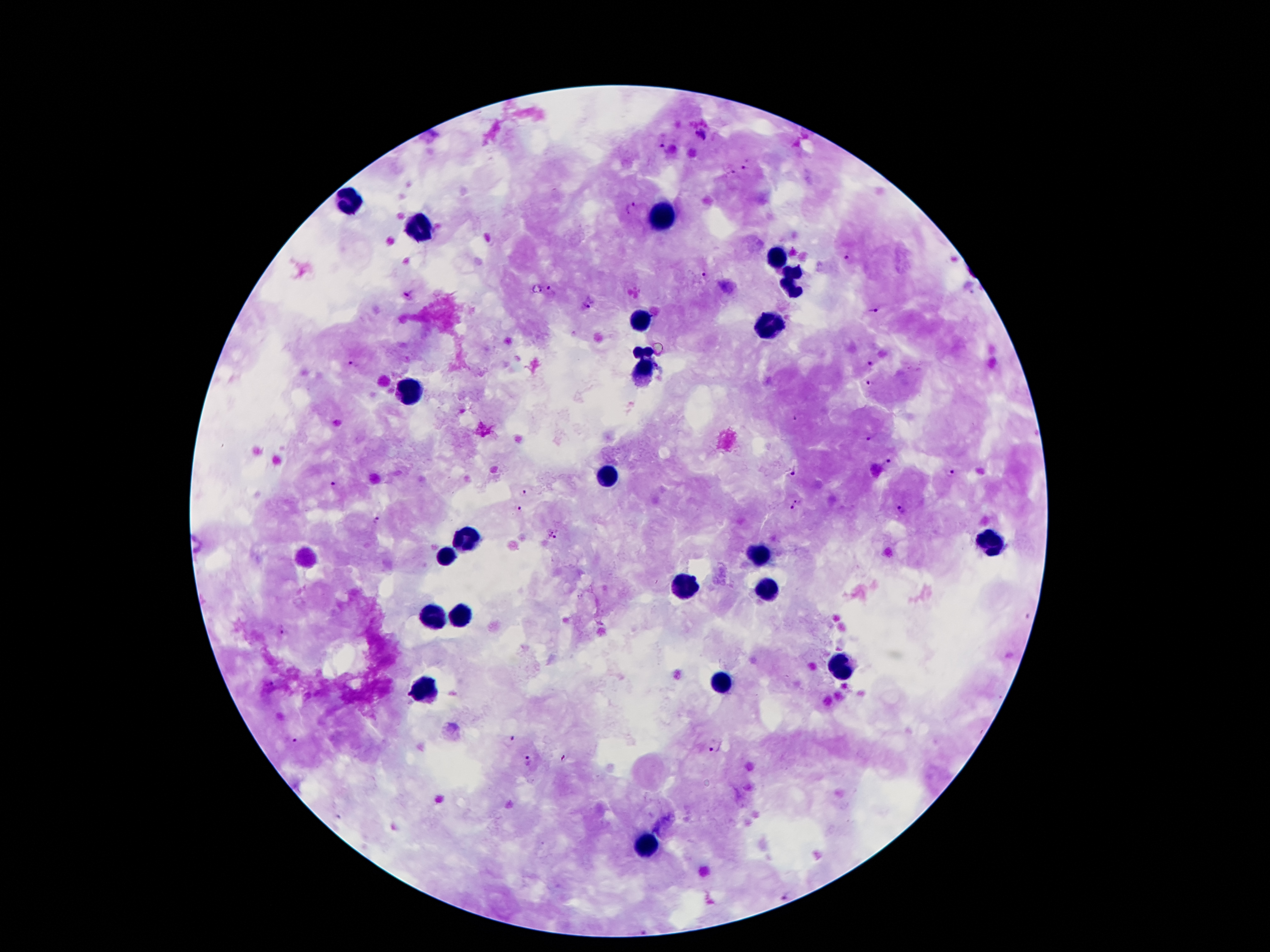
Approximate centers as {x, y} in pixels.
Summary:
  - Leukocyte locations: {349, 205}, {663, 218}, {417, 225}, {778, 257}, {797, 279}, {643, 320}, {771, 323}, {644, 373}, {414, 392}, {607, 479}, {467, 542}, {989, 545}, {758, 554}, {447, 557}, {679, 582}, {767, 587}, {435, 615}, {460, 615}, {847, 669}, {724, 682}, {426, 685}, {646, 845}
  - Malaria parasite locations: {700, 135}, {662, 145}, {744, 168}, {731, 171}, {631, 206}, {846, 257}, {704, 274}, {552, 291}, {407, 297}, {589, 304}, {873, 310}, {869, 363}, {353, 366}, {870, 385}, {795, 418}, {872, 438}, {886, 461}, {793, 469}, {951, 475}, {334, 487}, {523, 493}, {799, 500}, {518, 509}, {791, 509}, {900, 509}, {375, 521}, {551, 534}, {282, 632}, {267, 683}, {511, 739}, {292, 741}, {716, 747}, {564, 758}, {527, 761}, {785, 896}
  - Patient malaria status: infected with Plasmodium falciparum
  - Stain: Giemsa
  - Magnification: 100x
  - Image size: 1270×952 pixels
  - Capture: smartphone through the microscope eyepiece
  - Preparation: thick blood smear
  - Field of view: single